Locate every blood parasite and identify its species.
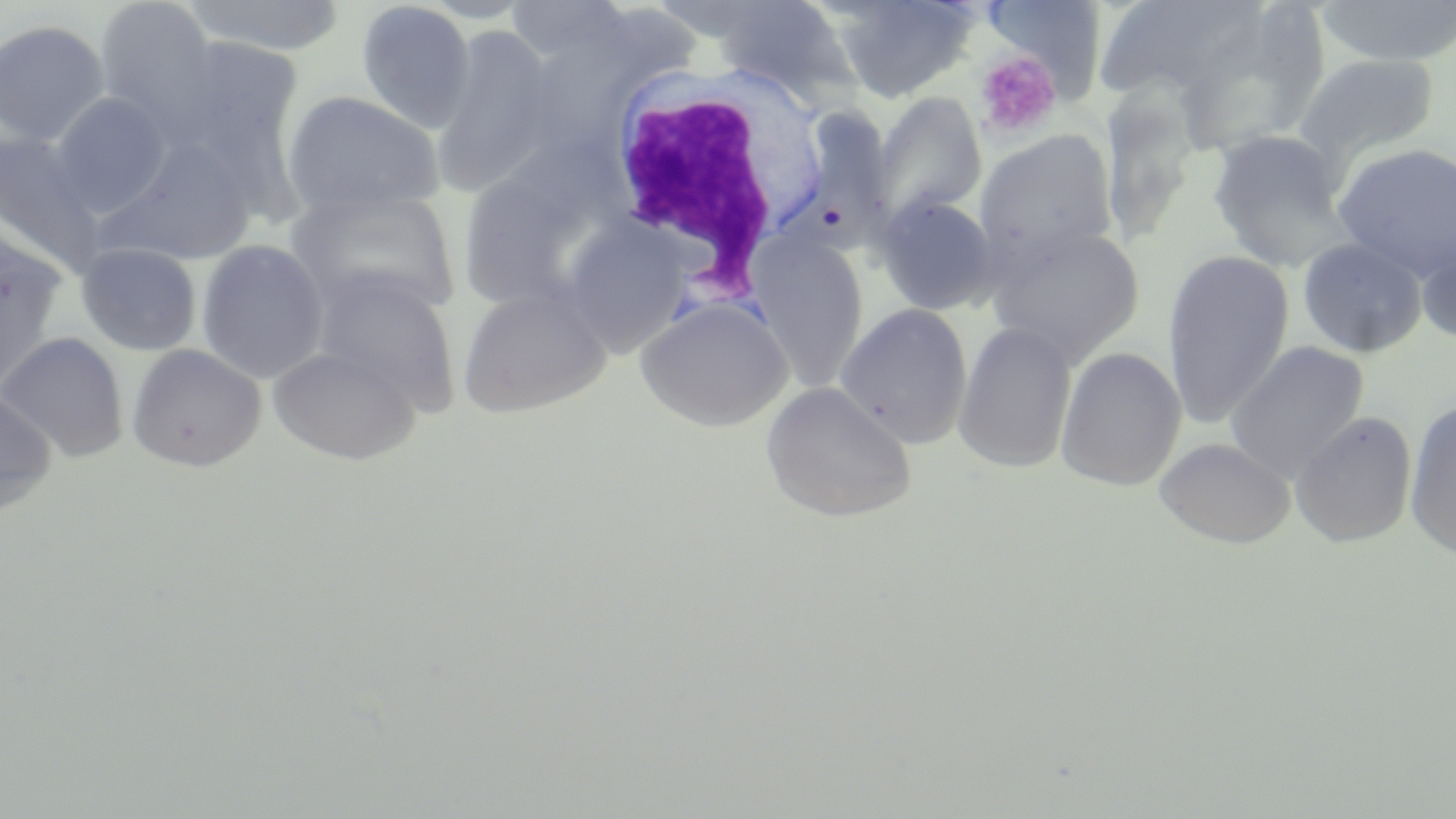

No blood parasites observed.

Summary:
  - Coordinate format: approximate bounding boxes as [x1, y1, x2, y2] in pixels
  - Uninfected red blood cell locations: [93, 0, 219, 135], [181, 0, 349, 57], [708, 0, 854, 102], [826, 0, 979, 102], [980, 0, 1108, 96], [1092, 0, 1273, 104], [1313, 0, 1456, 67], [355, 2, 475, 134], [503, 2, 637, 71], [0, 19, 111, 149], [431, 26, 561, 197], [158, 35, 307, 170], [1293, 53, 1441, 169], [280, 90, 444, 223], [871, 91, 987, 228], [49, 93, 171, 216], [785, 104, 897, 263], [1206, 129, 1354, 270], [974, 130, 1118, 266], [0, 131, 107, 271], [101, 139, 259, 266], [1332, 142, 1456, 283], [290, 186, 461, 319], [874, 194, 999, 317], [984, 220, 1146, 367], [557, 222, 693, 356], [0, 225, 68, 394], [1416, 228, 1456, 347], [747, 231, 869, 388], [1297, 237, 1428, 358], [196, 239, 329, 384], [76, 242, 201, 356], [1162, 251, 1295, 427], [309, 268, 461, 415], [456, 283, 613, 417], [635, 296, 792, 433], [834, 303, 973, 448], [953, 321, 1077, 475], [0, 332, 129, 463], [1226, 341, 1370, 482], [126, 344, 267, 472], [267, 345, 421, 465], [1055, 347, 1186, 492], [760, 381, 916, 523], [0, 388, 56, 518], [1404, 398, 1456, 561], [1290, 411, 1418, 548], [1155, 437, 1295, 549]
  - White blood cell locations: [599, 62, 825, 289]
  - Platelet locations: [974, 50, 1062, 139]
  - Slide-level diagnosis: negative for blood parasites
  - Field of view: single
  - Magnification: 1000x
  - Image size: 1456×819 pixels
  - Preparation: thin blood smear
  - Modality: optical microscopy
  - Stain: May-Grünwald-Giemsa